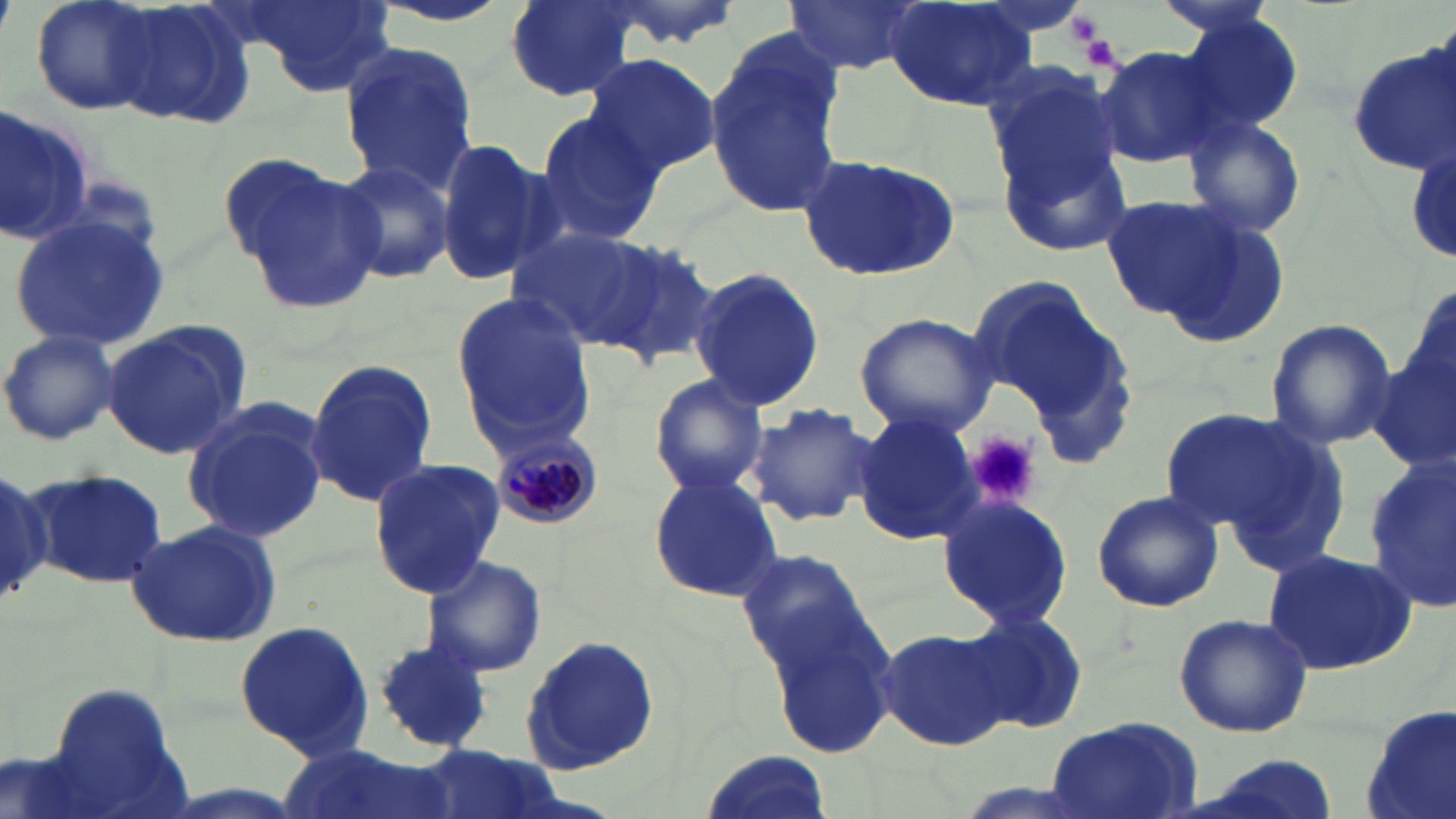

slide_level_diagnosis: Plasmodium malariae
modality: optical microscopy
image_size: 1456×819 pixels
stain: May-Grünwald-Giemsa
field_of_view: one of a larger specimen
magnification: 1000x
preparation: thin blood smear
platelet_locations: 'approximate bounding boxes as named x1/y1/x2/y2 corners in pixels: (x1=1065, y1=14, x2=1104, y2=46), (x1=1083, y1=33, x2=1123, y2=71), (x1=966, y1=431, x2=1041, y2=508)'
plasmodium_malariae_infected_red_blood_cell_locations: 'approximate bounding boxes as named x1/y1/x2/y2 corners in pixels: (x1=486, y1=427, x2=602, y2=530)'
uninfected_red_blood_cell_locations: 'approximate bounding boxes as named x1/y1/x2/y2 corners in pixels: (x1=30, y1=0, x2=163, y2=115), (x1=108, y1=0, x2=257, y2=132), (x1=366, y1=0, x2=520, y2=28), (x1=501, y1=0, x2=639, y2=102), (x1=592, y1=0, x2=744, y2=50), (x1=784, y1=0, x2=925, y2=78), (x1=1152, y1=0, x2=1284, y2=37), (x1=233, y1=1, x2=398, y2=97), (x1=884, y1=2, x2=1036, y2=111), (x1=1172, y1=11, x2=1305, y2=136), (x1=703, y1=29, x2=844, y2=220), (x1=336, y1=41, x2=479, y2=194), (x1=1093, y1=45, x2=1224, y2=170), (x1=1345, y1=45, x2=1456, y2=178), (x1=582, y1=51, x2=721, y2=176), (x1=982, y1=64, x2=1126, y2=239), (x1=0, y1=107, x2=94, y2=247), (x1=533, y1=111, x2=664, y2=246), (x1=1185, y1=116, x2=1308, y2=238), (x1=1405, y1=132, x2=1456, y2=271), (x1=435, y1=134, x2=556, y2=287), (x1=998, y1=139, x2=1135, y2=256), (x1=798, y1=150, x2=962, y2=283), (x1=227, y1=157, x2=383, y2=315), (x1=329, y1=158, x2=454, y2=284), (x1=1100, y1=193, x2=1251, y2=324), (x1=10, y1=215, x2=172, y2=353), (x1=1162, y1=217, x2=1288, y2=348), (x1=510, y1=223, x2=669, y2=351), (x1=584, y1=232, x2=721, y2=362), (x1=690, y1=265, x2=826, y2=412), (x1=966, y1=274, x2=1119, y2=422), (x1=449, y1=291, x2=596, y2=447), (x1=853, y1=312, x2=997, y2=438), (x1=1265, y1=318, x2=1397, y2=451), (x1=102, y1=324, x2=249, y2=462), (x1=1, y1=328, x2=122, y2=446), (x1=1370, y1=344, x2=1456, y2=473), (x1=302, y1=359, x2=439, y2=509), (x1=648, y1=373, x2=770, y2=496), (x1=180, y1=399, x2=331, y2=546), (x1=748, y1=402, x2=880, y2=527), (x1=1158, y1=405, x2=1320, y2=540), (x1=852, y1=410, x2=982, y2=546), (x1=1217, y1=427, x2=1352, y2=582), (x1=368, y1=458, x2=505, y2=598), (x1=1362, y1=458, x2=1456, y2=615), (x1=28, y1=466, x2=167, y2=590), (x1=0, y1=469, x2=59, y2=603), (x1=647, y1=473, x2=783, y2=603), (x1=1090, y1=490, x2=1224, y2=613), (x1=937, y1=492, x2=1075, y2=631), (x1=123, y1=519, x2=284, y2=647), (x1=1260, y1=549, x2=1419, y2=677), (x1=740, y1=552, x2=898, y2=747), (x1=420, y1=554, x2=548, y2=679), (x1=962, y1=610, x2=1090, y2=736), (x1=1173, y1=612, x2=1314, y2=738), (x1=234, y1=618, x2=376, y2=760), (x1=878, y1=625, x2=1012, y2=751), (x1=520, y1=634, x2=661, y2=774), (x1=371, y1=640, x2=492, y2=755), (x1=37, y1=682, x2=192, y2=818), (x1=1360, y1=707, x2=1456, y2=819), (x1=1042, y1=716, x2=1205, y2=819), (x1=281, y1=743, x2=456, y2=819), (x1=415, y1=744, x2=554, y2=819), (x1=702, y1=751, x2=830, y2=819), (x1=1185, y1=752, x2=1340, y2=819)'